Describe the morphology of the erythrocytes.
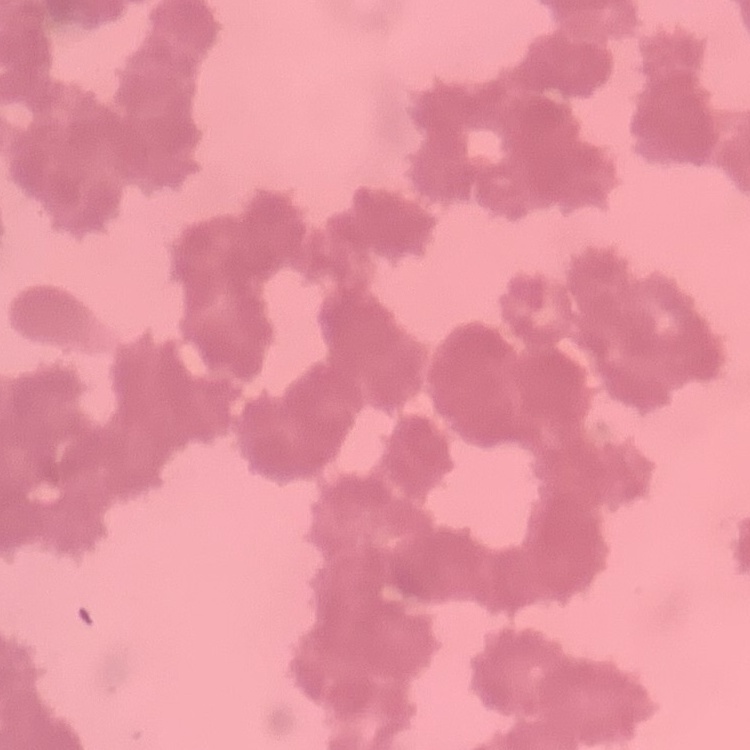
Rouleaux formation.

{
  "stain": "Field's or Giemsa",
  "preparation": "thin blood smear",
  "image_type": "one tile cut from a larger photomicrograph"
}